Report the malaria status of this cell.
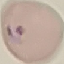

Parasitized.

Giemsa stain. Thin blood smear. Photographed with a smartphone camera at the microscope eyepiece. Cell patch, automatically extracted from a larger field of view and resized to 64 × 64 pixels.